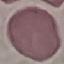

Summary:
  - Result: no malaria parasites seen
  - Preparation: thin blood film
  - Stain: Giemsa
  - Capture: smartphone camera at the microscope eyepiece
  - Image type: cell patch, automatically extracted from a larger field of view and resized to 64 × 64 pixels